Mark where platelets are.
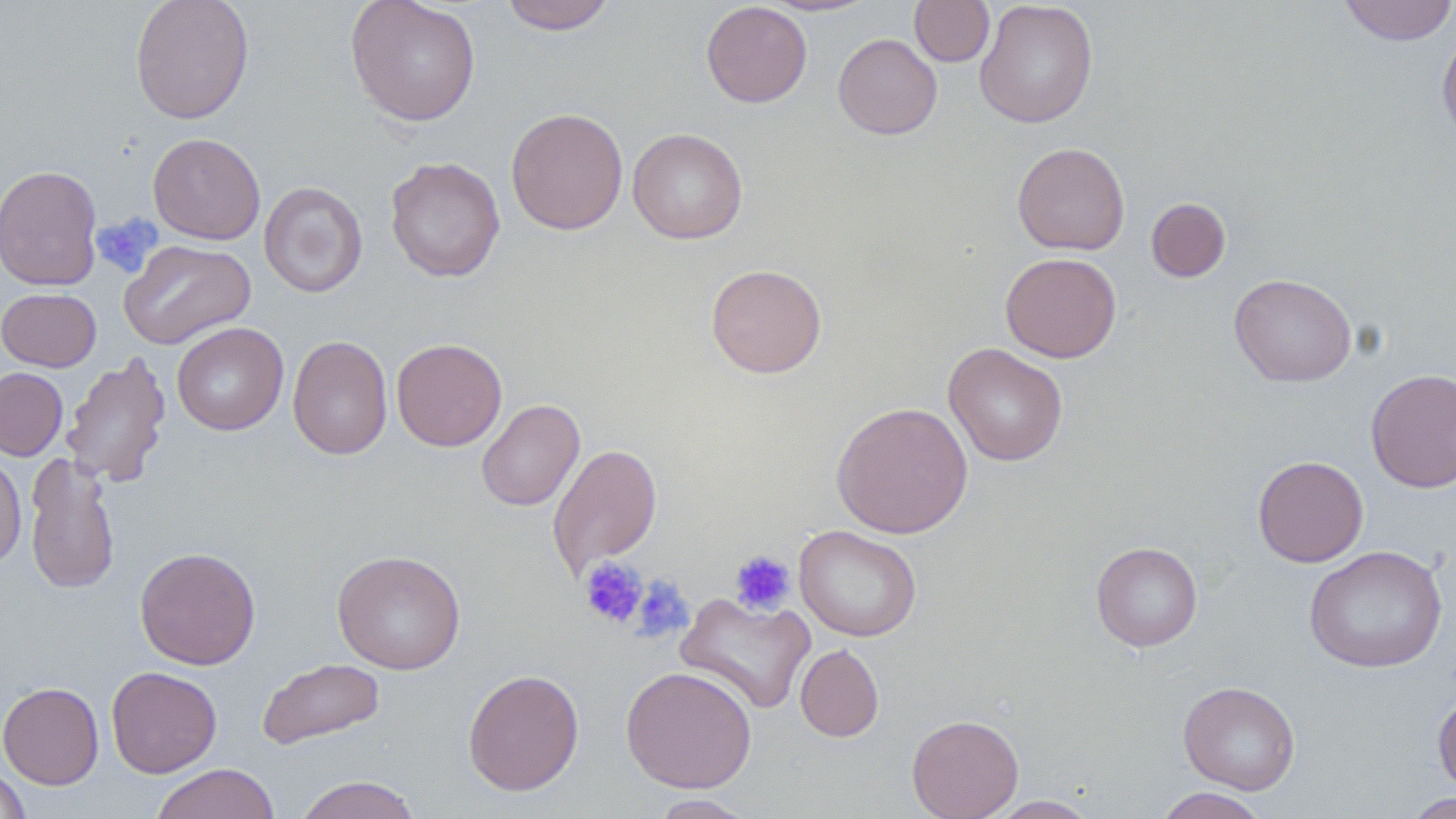
Approximate bounding boxes as (x1,y1)-(x2,y2) corner pairs in pixels.
Platelets: (91,213)-(164,278), (729,549)-(796,614), (578,557)-(648,628), (631,574)-(694,642).

{
  "slide_level_diagnosis": "negative for blood parasites",
  "magnification": "1000x",
  "stain": "May-Grünwald-Giemsa",
  "image_size": "1456×819 pixels",
  "field_of_view": "one of a larger specimen",
  "modality": "optical microscopy",
  "preparation": "thin blood smear",
  "uninfected_red_blood_cell_locations": "approximate bounding boxes as (x1,y1)-(x2,y2) corner pairs in pixels: (129,0)-(254,124), (344,0)-(482,126), (499,0)-(617,34), (975,0)-(1098,128), (1338,0)-(1456,45), (701,1)-(812,108), (764,1)-(876,16), (909,1)-(994,67), (1437,26)-(1456,145), (833,33)-(942,140), (505,108)-(629,235), (627,127)-(748,244), (148,132)-(266,244), (1012,142)-(1130,255), (385,156)-(505,282), (0,164)-(104,291), (259,181)-(368,297), (1146,197)-(1231,282), (119,239)-(256,349), (1000,252)-(1122,363), (705,263)-(827,379), (1229,273)-(1357,387), (0,288)-(101,371), (172,322)-(289,435), (288,335)-(391,461), (391,337)-(507,451), (944,343)-(1068,466), (61,352)-(172,488), (0,367)-(68,461), (1365,368)-(1456,493), (476,398)-(585,512), (832,401)-(973,538), (548,443)-(662,578), (0,453)-(27,570), (24,453)-(121,595), (1252,455)-(1368,567), (794,525)-(922,642), (1091,542)-(1203,651), (1304,545)-(1448,673), (134,547)-(261,670), (332,550)-(466,674), (675,592)-(815,714), (795,644)-(884,742), (257,658)-(385,749), (106,666)-(222,778), (620,666)-(757,793), (462,668)-(584,796), (1178,680)-(1300,794), (0,681)-(104,789), (1432,690)-(1456,796), (906,714)-(1023,819), (150,763)-(281,819), (0,764)-(31,819), (292,775)-(423,819), (1151,787)-(1270,818), (1402,792)-(1455,818), (649,794)-(757,818), (986,795)-(1101,818)"
}